State the blood parasite species.
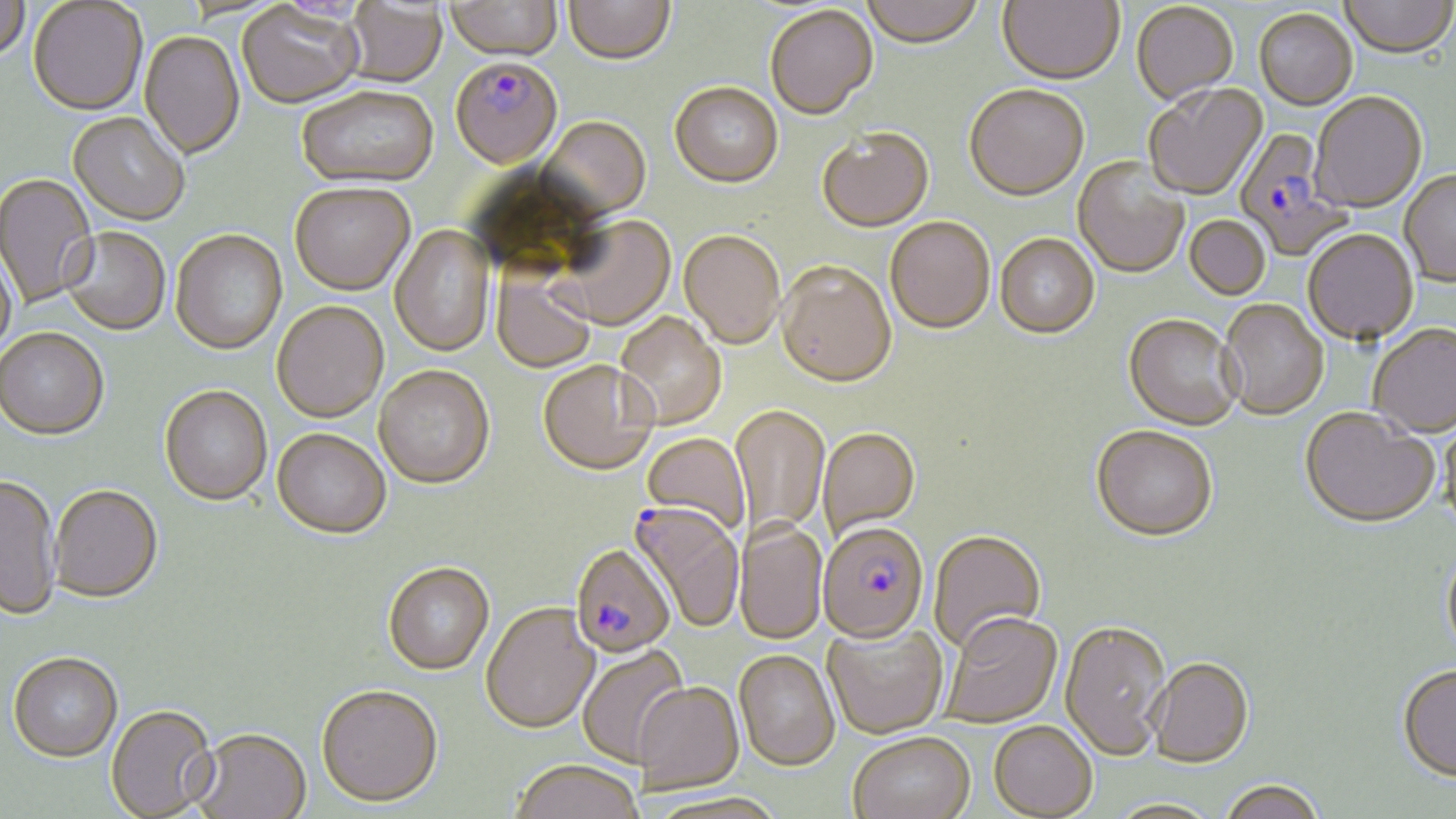
Plasmodium falciparum.

Approximate bounding boxes as (x1,y1)-(x2,y2) corner pairs in pixels. Uninfected red blood cell locations: (0,0)-(29,67), (446,0)-(563,64), (564,0)-(676,68), (860,0)-(984,51), (997,0)-(1124,88), (1339,0)-(1455,61), (28,1)-(147,116), (343,1)-(449,89), (237,4)-(364,111), (1131,4)-(1239,109), (765,7)-(878,123), (1255,11)-(1357,112), (139,32)-(245,162), (669,85)-(783,191), (1143,85)-(1268,202), (964,87)-(1089,204), (296,89)-(439,192), (1311,94)-(1427,215), (68,114)-(189,228), (538,119)-(651,223), (817,131)-(935,235), (1071,157)-(1190,281), (1400,172)-(1456,289), (0,174)-(99,310), (290,186)-(415,298), (1184,217)-(1270,301), (553,218)-(676,333), (884,219)-(995,337), (390,225)-(496,358), (61,229)-(170,336), (170,231)-(288,356), (1303,232)-(1419,348), (679,233)-(785,351), (995,236)-(1100,342), (0,251)-(17,361), (776,265)-(897,392), (491,273)-(596,374), (272,302)-(389,424), (1217,302)-(1328,422), (614,313)-(726,431), (1123,316)-(1242,433), (1368,327)-(1456,440), (0,329)-(109,441), (538,361)-(658,478), (373,366)-(495,491), (158,385)-(272,507), (730,405)-(830,541), (1300,411)-(1439,531), (1438,416)-(1456,533), (817,428)-(921,542), (272,429)-(392,540), (1091,429)-(1217,546), (641,434)-(750,536), (0,474)-(61,620), (49,485)-(163,603), (736,522)-(827,646), (928,532)-(1047,654), (1441,551)-(1456,662), (383,563)-(494,675), (480,603)-(600,735), (941,615)-(1062,730), (822,621)-(949,740), (1059,623)-(1171,764), (577,644)-(691,769), (7,651)-(122,762), (734,651)-(840,773), (1148,660)-(1253,770), (1397,666)-(1456,783), (633,684)-(744,795), (316,688)-(444,810), (106,706)-(219,819), (988,723)-(1097,819), (192,730)-(311,819), (849,733)-(975,819), (510,761)-(644,819), (1219,782)-(1326,819), (644,794)-(788,819). Plasmodium falciparum-infected red blood cell locations: (450,60)-(563,172), (1235,128)-(1351,260), (629,502)-(745,634), (818,525)-(930,647), (571,544)-(676,658). Image is 1456×819 pixels. One field of a larger specimen. May-Grünwald-Giemsa-stained preparation. Thin blood film. Optical microscopy. 1000x magnification.